State the preparation type.
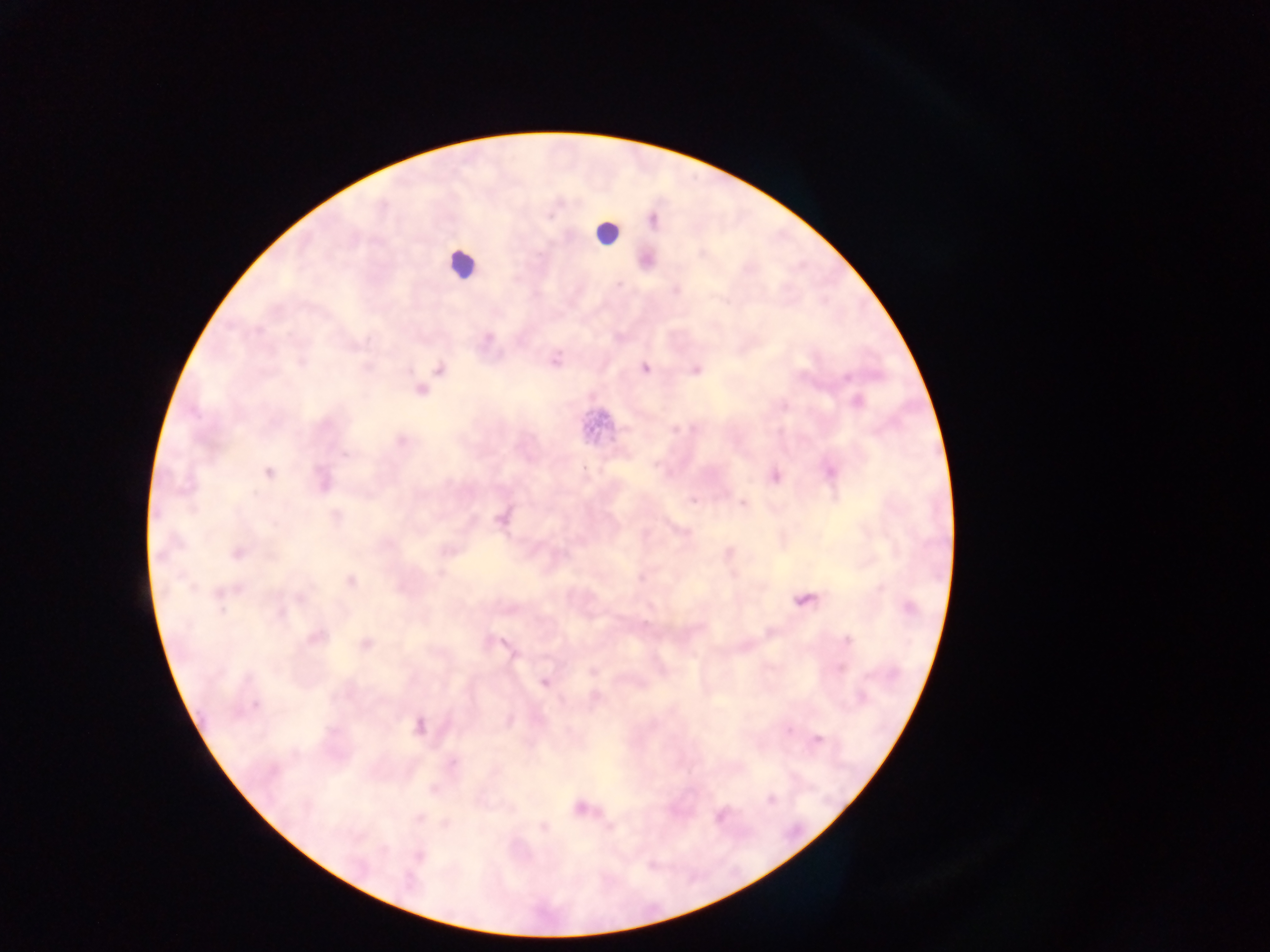
This is a thick smear.

{
  "malaria_parasite_locations": "approximate centers as (x, y) in pixels: (653, 221), (488, 337), (556, 361), (645, 368), (440, 369), (695, 370), (847, 377), (421, 390), (857, 402), (675, 428), (401, 441), (344, 454), (831, 472), (268, 473), (775, 477), (693, 500), (743, 503), (337, 515), (237, 553), (441, 573), (641, 578), (351, 580), (238, 589), (299, 598), (804, 599), (910, 607), (221, 610), (280, 615), (315, 638), (847, 641), (366, 644), (507, 646), (592, 671), (544, 683), (255, 704), (419, 726), (789, 730), (818, 739), (452, 763), (432, 790), (771, 800), (581, 808), (721, 816), (419, 817), (543, 827), (418, 856)",
  "country": "Ghana",
  "image_size": "1270×952 pixels",
  "field_of_view": "single",
  "capture": "mobile-phone photograph through a microscope",
  "leukocyte_locations": "approximate centers as (x, y) in pixels: (606, 232), (461, 264)"
}